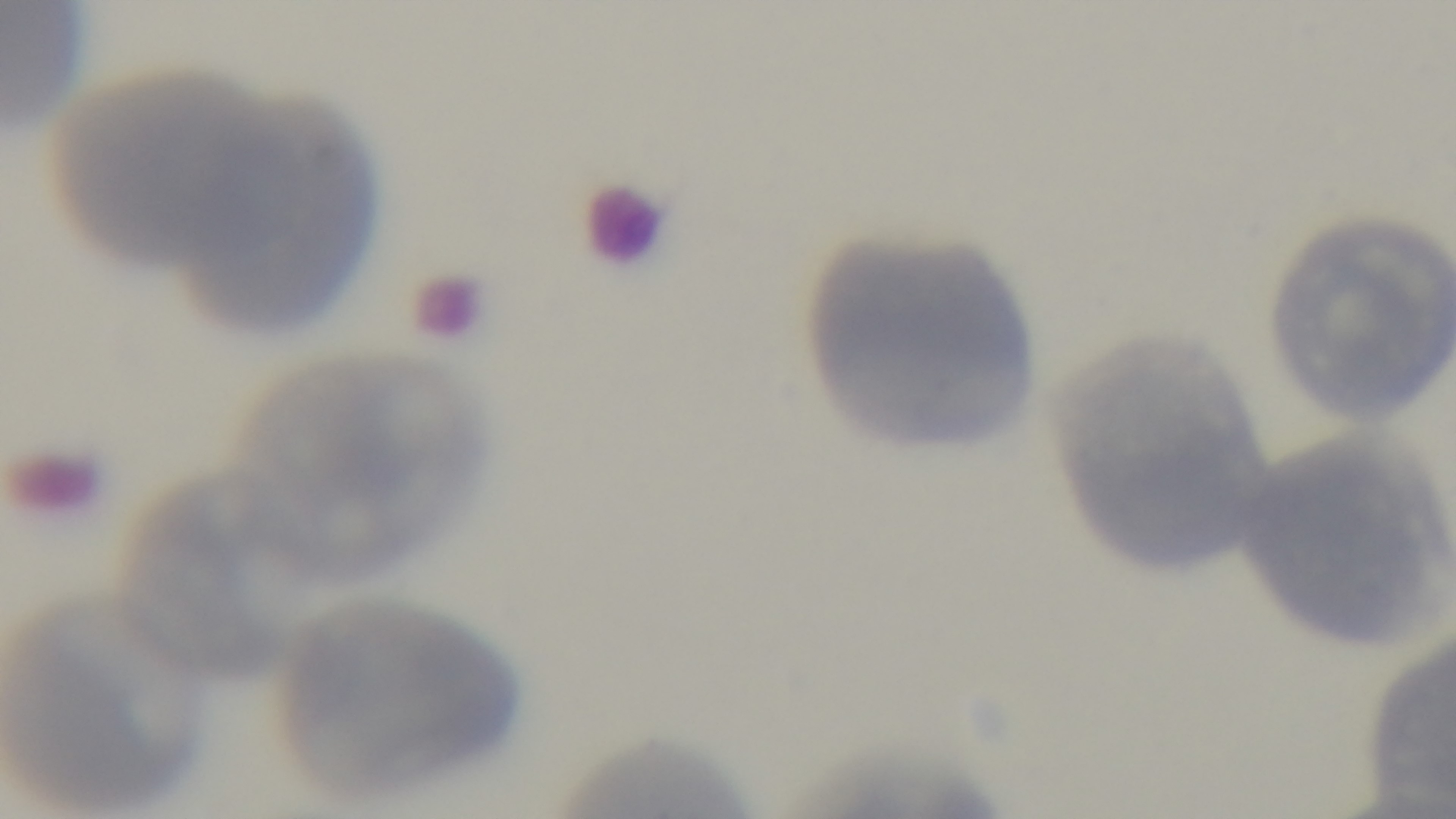
malaria_status: uninfected
stain: Giemsa
field_of_view: one from the slide
capture: mounted 4K digital camera
modality: light microscopy
objective: 100x oil immersion
preparation: thin blood film